State the blood parasite species.
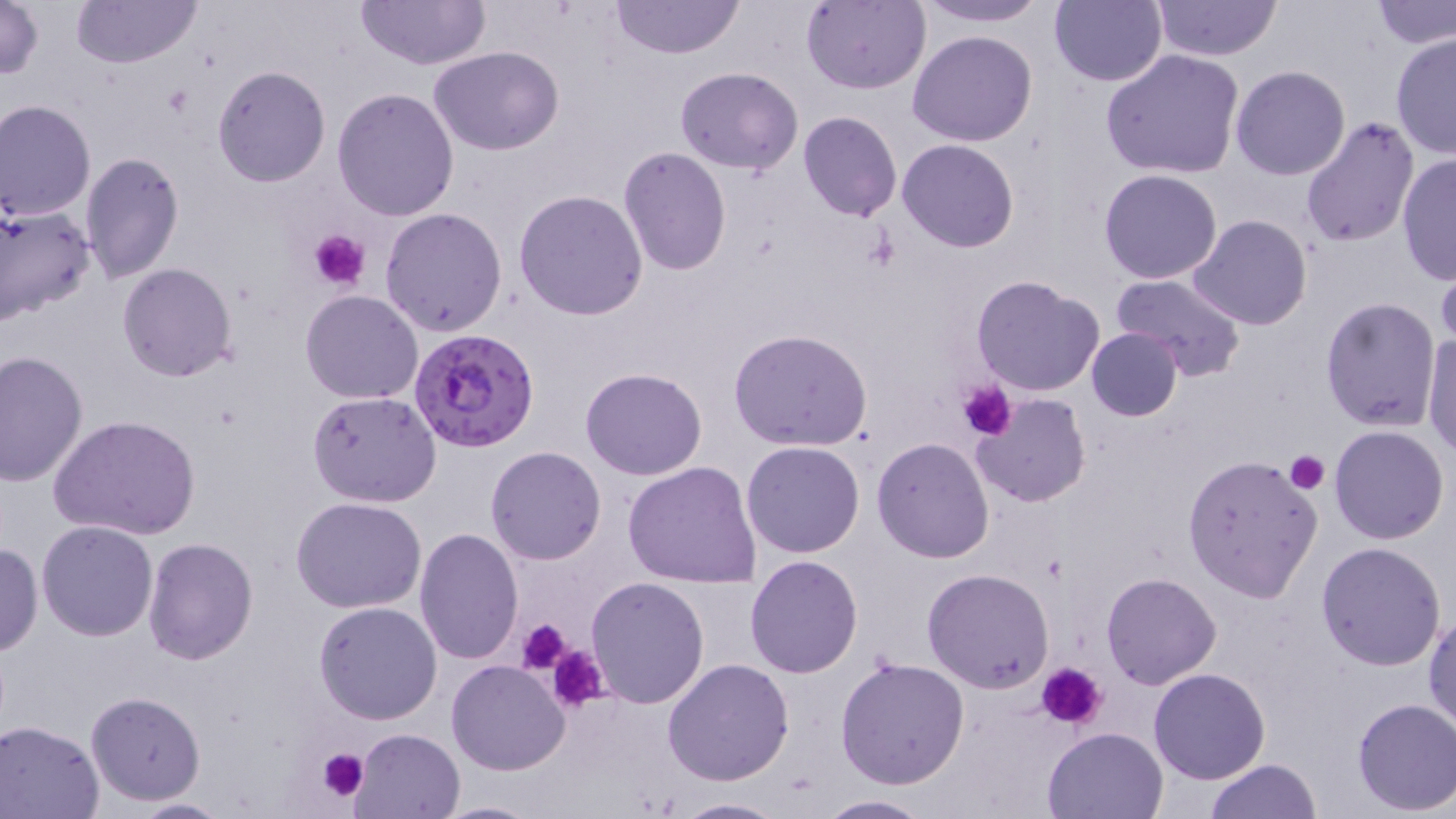

Plasmodium falciparum.

Approximate bounding boxes as (x1, y1, x2, y2) in pixels. Plasmodium falciparum-infected red blood cell locations: (411, 327, 540, 452). Uninfected red blood cell locations: (1, 0, 44, 83), (71, 0, 202, 70), (610, 0, 744, 59), (913, 0, 1050, 27), (1371, 0, 1455, 50), (356, 1, 491, 70), (799, 1, 931, 94), (1049, 1, 1167, 86), (1150, 1, 1282, 60), (909, 30, 1038, 147), (1390, 33, 1456, 159), (429, 45, 563, 155), (1101, 48, 1246, 179), (211, 65, 331, 186), (1230, 65, 1352, 180), (676, 67, 804, 175), (331, 87, 459, 222), (0, 100, 96, 220), (798, 111, 903, 222), (1299, 115, 1420, 248), (898, 139, 1020, 254), (617, 146, 732, 276), (80, 151, 186, 285), (1397, 155, 1455, 283), (1098, 169, 1222, 284), (514, 190, 648, 321), (0, 201, 95, 325), (380, 208, 509, 337), (1188, 214, 1312, 330), (117, 263, 237, 382), (1436, 269, 1456, 353), (1111, 274, 1247, 382), (970, 275, 1106, 397), (299, 291, 423, 404), (1319, 296, 1441, 432), (728, 327, 873, 451), (1085, 328, 1182, 422), (1423, 329, 1456, 460), (0, 350, 87, 485), (580, 367, 708, 480), (307, 391, 443, 508), (970, 393, 1092, 509), (49, 414, 201, 540), (1330, 425, 1450, 545), (871, 438, 995, 563), (741, 440, 866, 558), (486, 446, 606, 565), (1181, 453, 1324, 602), (623, 461, 764, 589), (291, 496, 425, 613), (35, 520, 159, 641), (413, 528, 525, 666), (142, 536, 260, 665), (1315, 541, 1447, 670), (0, 542, 43, 657), (745, 554, 862, 677), (922, 568, 1055, 694), (1100, 572, 1222, 690), (586, 575, 710, 707), (313, 601, 442, 724), (1424, 610, 1456, 734), (835, 657, 970, 791), (446, 658, 571, 776), (663, 658, 795, 787), (1149, 667, 1270, 783), (84, 691, 207, 806), (1351, 698, 1456, 816), (1, 720, 104, 818), (1043, 726, 1169, 818), (351, 728, 467, 819), (1205, 759, 1323, 818), (815, 792, 934, 817), (670, 795, 789, 819), (118, 797, 237, 817), (429, 799, 543, 818). Platelet locations: (308, 228, 369, 291), (957, 380, 1017, 439), (1285, 451, 1329, 493), (517, 617, 575, 673), (546, 642, 609, 712), (1038, 663, 1106, 731), (315, 747, 369, 804). Single field of view. Light microscopy. Captured at 1000x magnification. Image is 1456×819 pixels. May-Grünwald-Giemsa-stained preparation. Thin blood film.